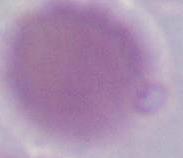
Summary:
  - Magnification: 1000x
  - Identification: erythrocyte
  - Modality: photomicrograph